Give the position of every Plasmodium parasite visible.
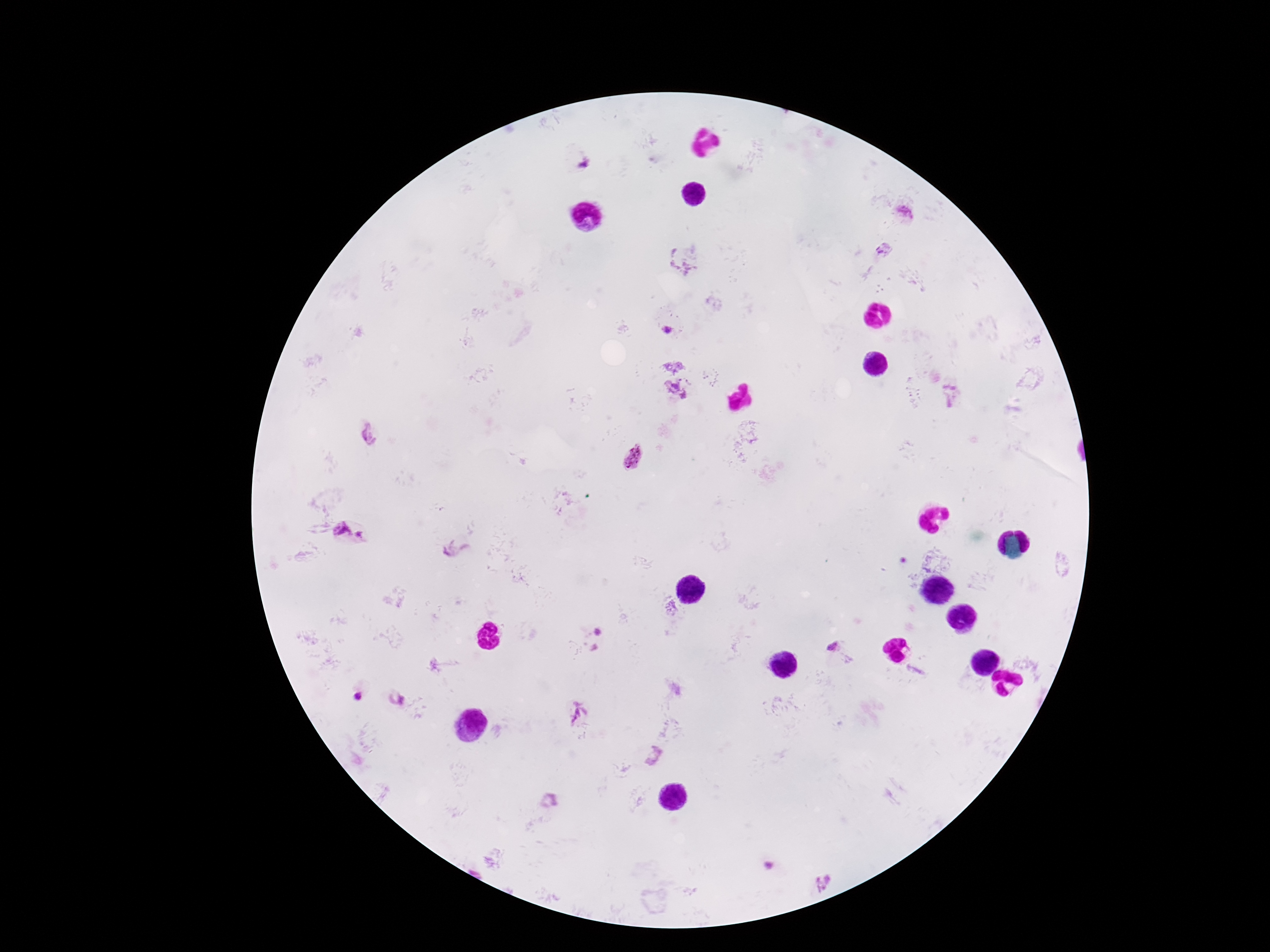
Approximate centers as {x, y} in pixels.
Plasmodium parasites: {586, 165}, {905, 215}, {883, 249}, {679, 265}, {666, 330}, {370, 433}, {633, 457}, {342, 531}, {361, 535}, {598, 632}, {832, 646}, {357, 697}, {395, 697}, {577, 714}, {654, 755}, {770, 866}, {824, 883}.

Summary:
  - Field of view: one from this slide
  - Capture: smartphone camera through the microscope eyepiece
  - Magnification: 100x
  - Preparation: thick blood film
  - Image size: 1270×952 pixels
  - Stain: Giemsa
  - Patient malaria status: positive